Assess this cell for malaria.
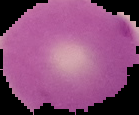
It is uninfected.

image type = segmented cell region with the area outside set to black
preparation = thin blood film
image size = 139×115 pixels